Identify the parasite.
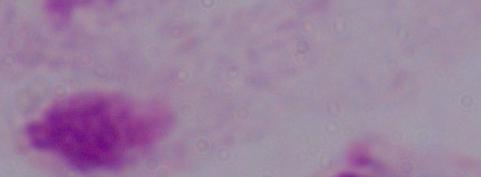

A trichomonad.

modality = micrograph
magnification = 1000x